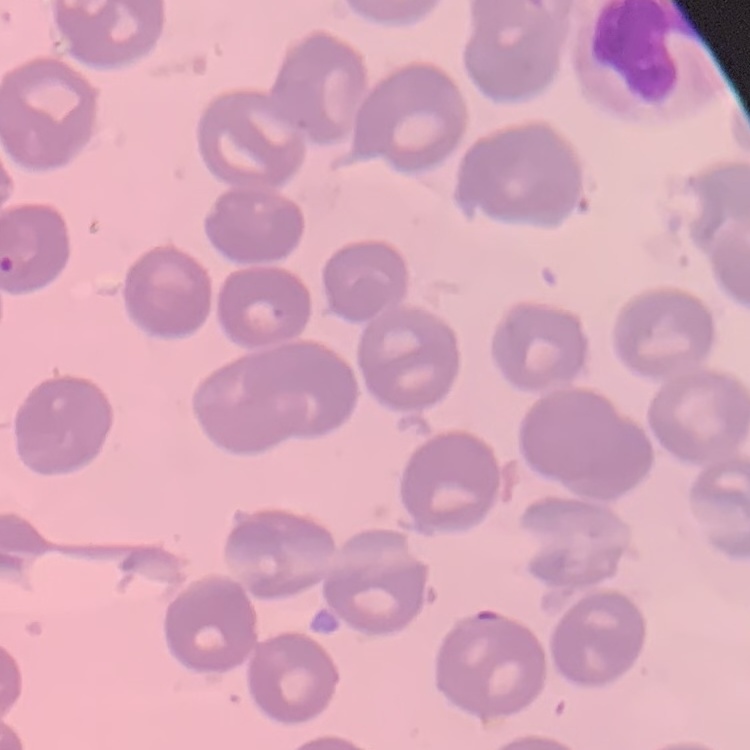

Summary:
  - Red blood cell morphology: no rouleaux formation
  - Preparation: thin blood smear
  - Image type: one tile cut from a larger photomicrograph
  - Stain: Field's or Giemsa